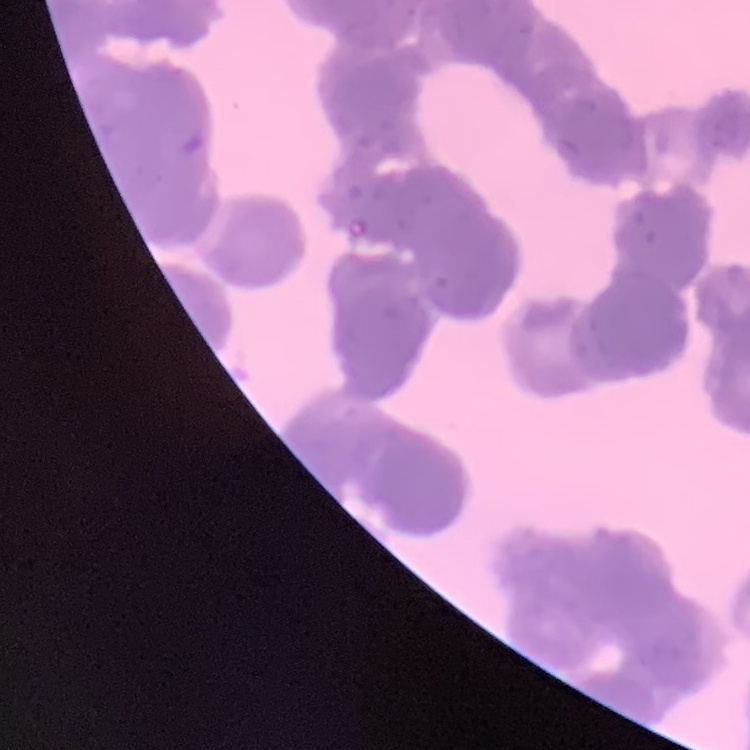

Summary:
  - Erythrocyte morphology: rouleaux formation
  - Stain: Field's or Giemsa
  - Preparation: thin peripheral smear
  - Image type: one tile cut from a larger photomicrograph